Classify this cell by malaria status.
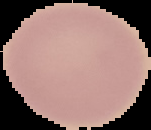
Uninfected.

{
  "image_size": "151×130 pixels",
  "image_type": "segmented cell region with the area outside set to black",
  "preparation": "thin blood smear"
}